Give the extent of all uninfected red blood cells.
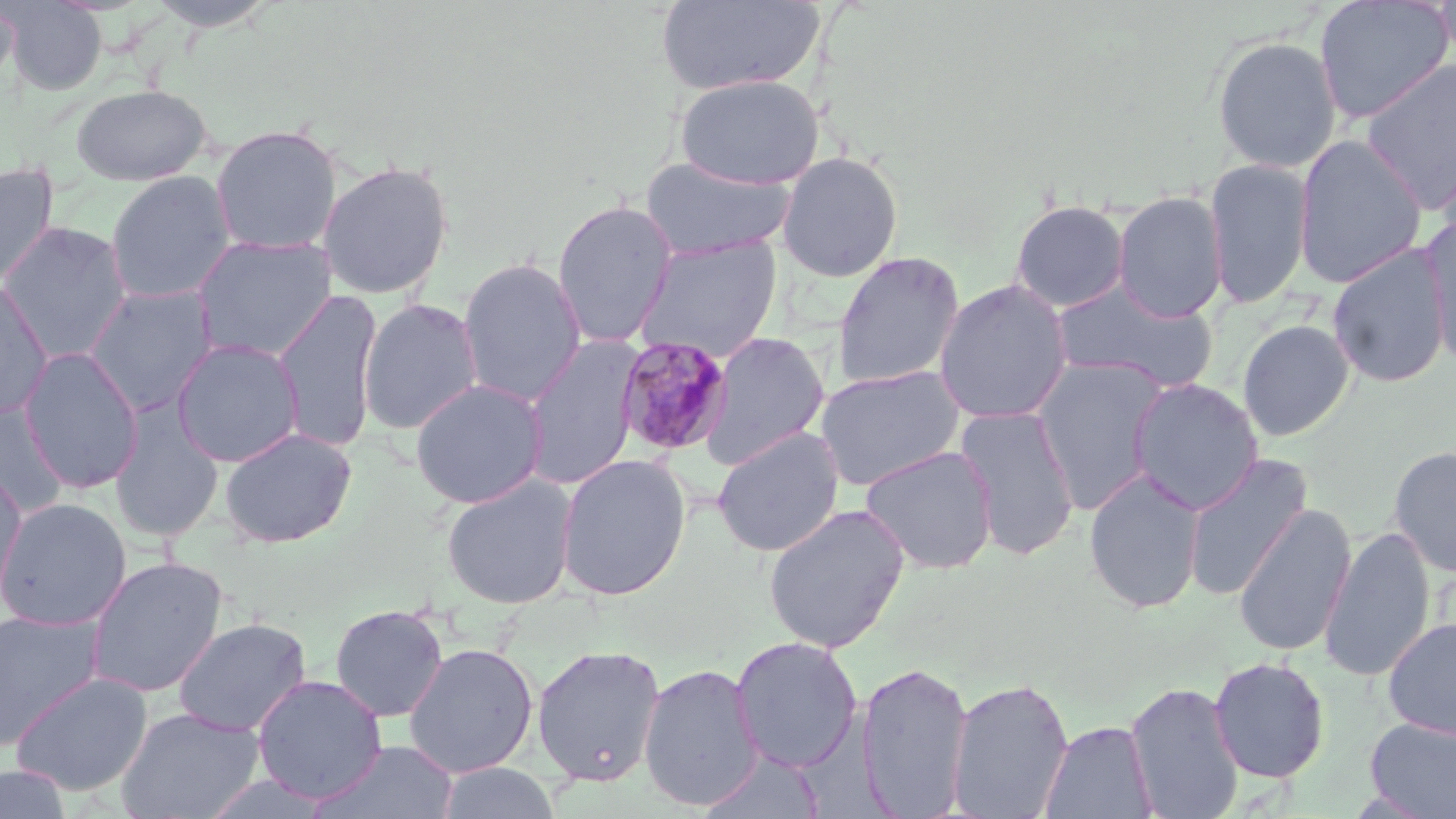

Approximate bounding boxes as (x1, y1, x2, y2) in pixels.
Uninfected red blood cells: (3, 0, 107, 95), (657, 0, 823, 95), (1314, 0, 1453, 124), (1434, 0, 1456, 67), (0, 1, 20, 95), (143, 1, 280, 31), (1211, 35, 1342, 173), (1360, 59, 1456, 214), (673, 74, 825, 190), (70, 84, 212, 185), (210, 123, 342, 255), (1293, 134, 1428, 289), (775, 150, 904, 282), (638, 154, 798, 261), (1205, 157, 1314, 309), (317, 160, 454, 299), (0, 163, 59, 286), (105, 171, 236, 305), (1112, 191, 1228, 323), (551, 199, 679, 348), (1009, 199, 1131, 312), (1419, 213, 1456, 368), (0, 221, 133, 362), (192, 234, 337, 362), (632, 236, 782, 362), (1327, 243, 1451, 387), (831, 251, 965, 389), (457, 257, 587, 407), (0, 276, 53, 419), (934, 279, 1073, 424), (1052, 279, 1218, 394), (84, 284, 218, 415), (274, 289, 381, 454), (358, 298, 484, 435), (1237, 319, 1355, 441), (699, 332, 831, 470), (521, 335, 644, 490), (171, 338, 305, 468), (18, 347, 144, 493), (1032, 357, 1169, 515), (814, 364, 965, 491), (410, 378, 548, 508), (1127, 378, 1264, 514), (0, 401, 70, 518), (109, 403, 225, 542), (955, 404, 1081, 561), (711, 426, 845, 557), (219, 427, 358, 547), (860, 445, 999, 574), (1388, 445, 1456, 578), (1182, 452, 1312, 601), (555, 453, 692, 601), (1084, 468, 1206, 613), (0, 474, 28, 609), (440, 475, 578, 609), (0, 497, 131, 631), (1232, 501, 1357, 658), (762, 502, 910, 654), (1319, 527, 1436, 682), (86, 556, 228, 698), (330, 603, 448, 722), (0, 610, 105, 749), (172, 617, 312, 737), (1382, 617, 1456, 738), (729, 636, 863, 774), (403, 642, 539, 778), (531, 644, 666, 787), (1208, 656, 1330, 783), (855, 661, 974, 817), (639, 663, 763, 812), (11, 671, 153, 796), (252, 674, 388, 804), (946, 676, 1075, 818), (1124, 681, 1245, 818), (115, 706, 265, 818), (1363, 717, 1456, 819), (1039, 719, 1158, 818), (311, 739, 459, 819), (697, 750, 826, 818), (435, 762, 562, 819), (0, 765, 71, 818).

slide-level diagnosis = Plasmodium malariae
image size = 1456×819 pixels
preparation = thin blood film
field of view = one of a larger specimen
modality = light microscopy
magnification = 1000x
stain = May-Grünwald-Giemsa
Plasmodium malariae-infected red blood cell locations = approximate bounding boxes as (x1, y1, x2, y2) in pixels: (615, 335, 734, 458)